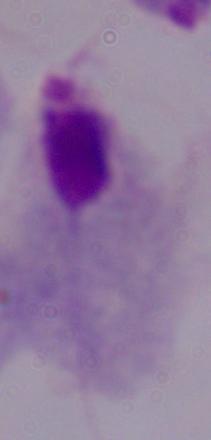

Summary:
  - Modality: photomicrograph
  - Identification: trichomonad
  - Magnification: 1000x